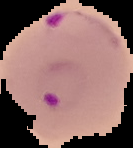
Summary:
  - Result: malaria parasites detected
  - Image type: segmented cell region on a black background
  - Preparation: thin blood smear
  - Image size: 133×148 pixels